Locate every leukocyte (white blood cell).
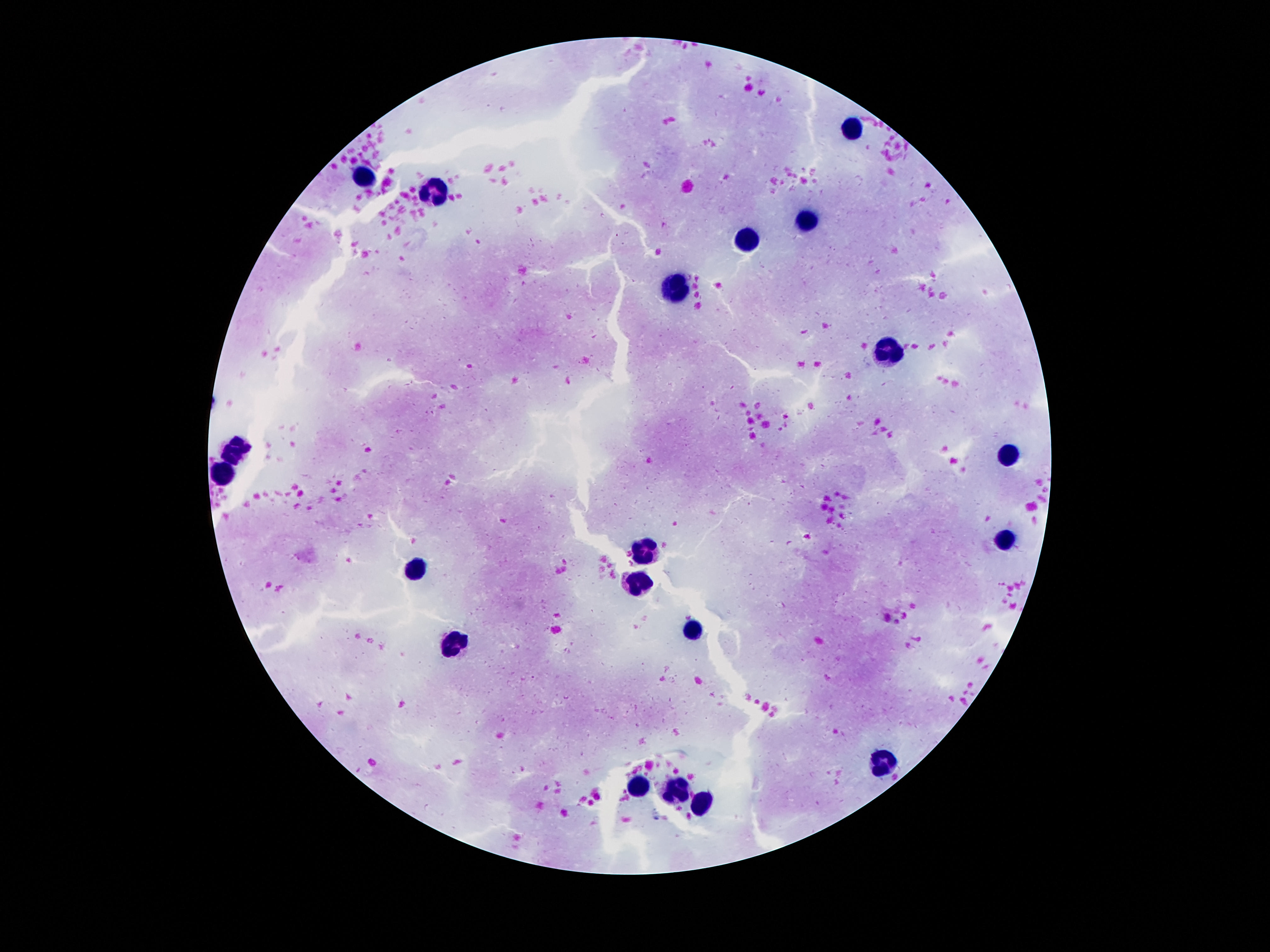

Approximate centers as {x, y} in pixels.
Leukocytes: {857, 128}, {363, 178}, {433, 190}, {806, 219}, {747, 237}, {679, 290}, {888, 350}, {236, 449}, {1013, 455}, {224, 473}, {1007, 541}, {640, 553}, {417, 568}, {636, 582}, {693, 629}, {456, 642}, {884, 760}, {636, 787}, {677, 793}, {704, 804}.

100x magnification. One field from this slide. Thick blood film. Image is 1270×952 pixels. Giemsa stain. Patient malaria status: uninfected. Photographed through the microscope eyepiece with a smartphone camera.